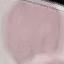

malaria status = uninfected
capture = smartphone camera at the microscope eyepiece
stain = Giemsa
image type = automatically extracted cell patch, resized to 64 × 64 pixels
preparation = thin blood film